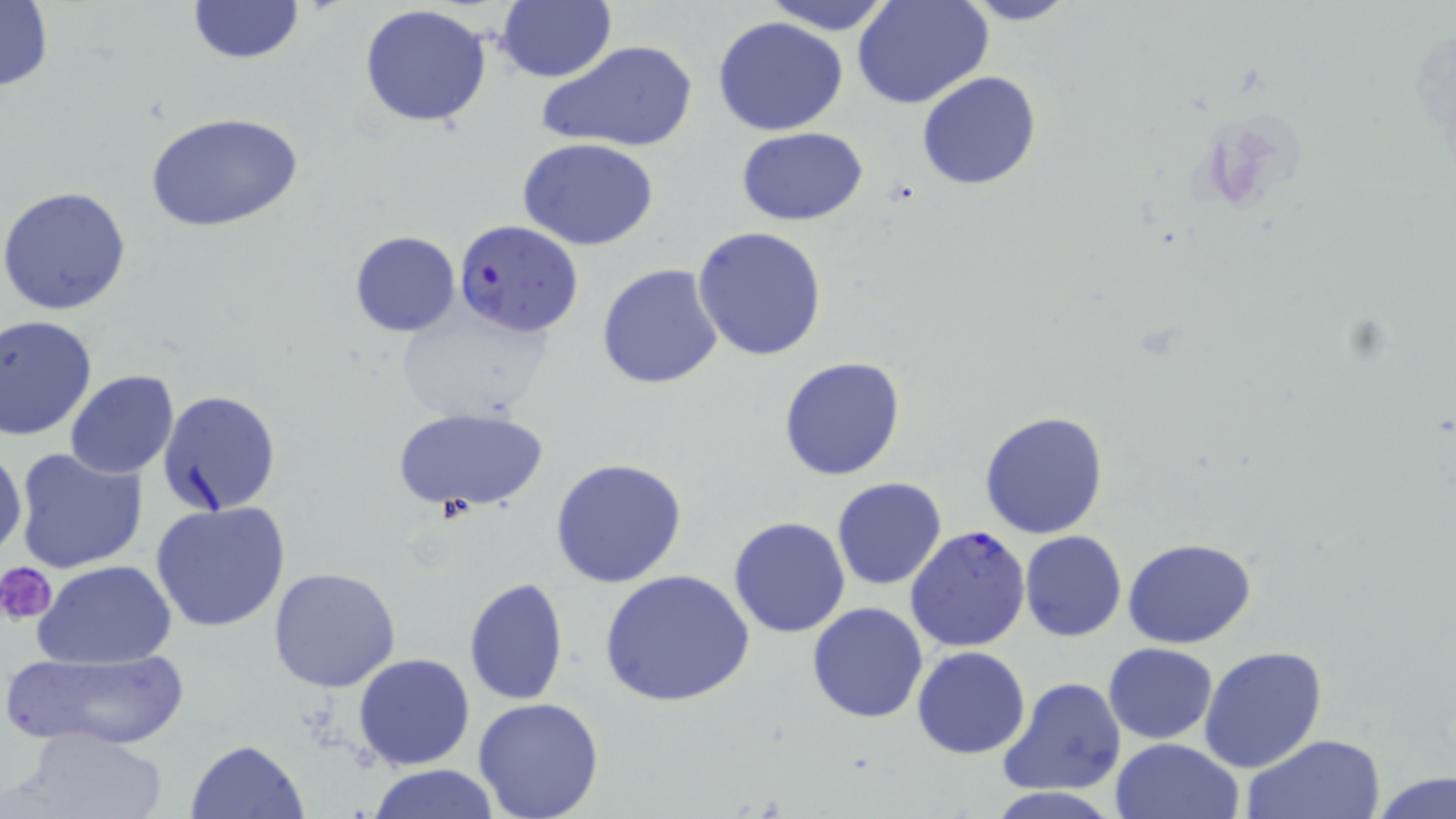

Approximate bounding boxes as [x1, y1, x2, y2] in pixels. Platelet locations: [0, 562, 57, 624]. Uninfected red blood cell locations: [497, 0, 616, 83], [759, 0, 899, 34], [954, 0, 1085, 26], [0, 1, 53, 92], [189, 1, 303, 65], [854, 1, 992, 109], [359, 5, 493, 129], [714, 16, 849, 136], [536, 38, 699, 153], [916, 71, 1042, 191], [144, 111, 304, 234], [736, 127, 872, 226], [517, 138, 662, 252], [0, 187, 132, 315], [692, 226, 828, 362], [350, 229, 460, 335], [596, 263, 726, 389], [392, 300, 554, 421], [0, 315, 98, 441], [778, 355, 907, 482], [65, 371, 179, 477], [157, 390, 282, 518], [391, 405, 551, 515], [979, 410, 1111, 540], [0, 442, 24, 561], [12, 446, 149, 576], [549, 457, 692, 590], [831, 477, 948, 591], [151, 501, 293, 633], [729, 516, 851, 638], [1019, 530, 1127, 642], [1123, 538, 1256, 649], [34, 559, 177, 667], [268, 567, 402, 693], [599, 567, 755, 709], [463, 577, 568, 704], [806, 601, 928, 723], [1104, 642, 1217, 744], [913, 646, 1030, 759], [1199, 646, 1330, 774], [5, 647, 191, 749], [354, 653, 474, 770], [999, 676, 1127, 797], [472, 698, 605, 819], [15, 724, 169, 818], [1242, 732, 1386, 819], [1109, 737, 1244, 819], [187, 739, 309, 818], [366, 765, 500, 819], [1373, 771, 1455, 819]. Plasmodium falciparum-infected red blood cell locations: [454, 218, 583, 337], [905, 526, 1031, 651]. Slide-level diagnosis: Plasmodium falciparum. Image is 1456×819 pixels. 1000x magnification. Optical microscopy. One field of a larger specimen. May-Grünwald-Giemsa-stained preparation. Thin blood film.